Look for parasitized red blood cells.
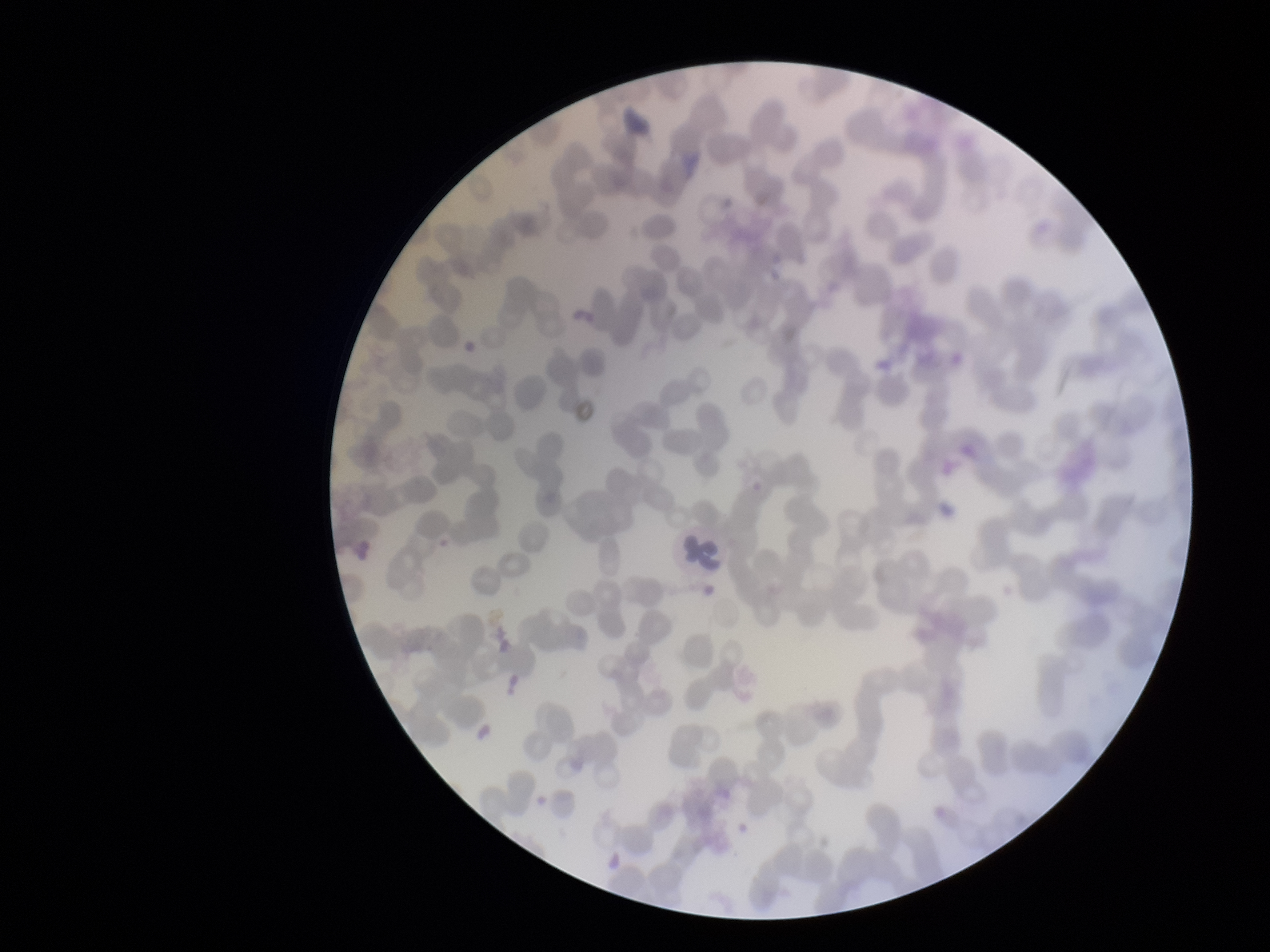

None seen.

Summary:
  - Stain: Giemsa
  - Red blood cell count: 263
  - Field of view: single
  - Image size: 1270×952 pixels
  - Patient malaria status: negative
  - Capture: smartphone photograph through the microscope eyepiece
  - Preparation: thin
  - Parasitized red blood cell count: 0